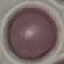
Result: no malaria parasites seen. Giemsa stain. Thin smear of blood. Acquired by smartphone through the microscope eyepiece. Cell patch, automatically extracted from a larger field of view and resized to 64 × 64 pixels.